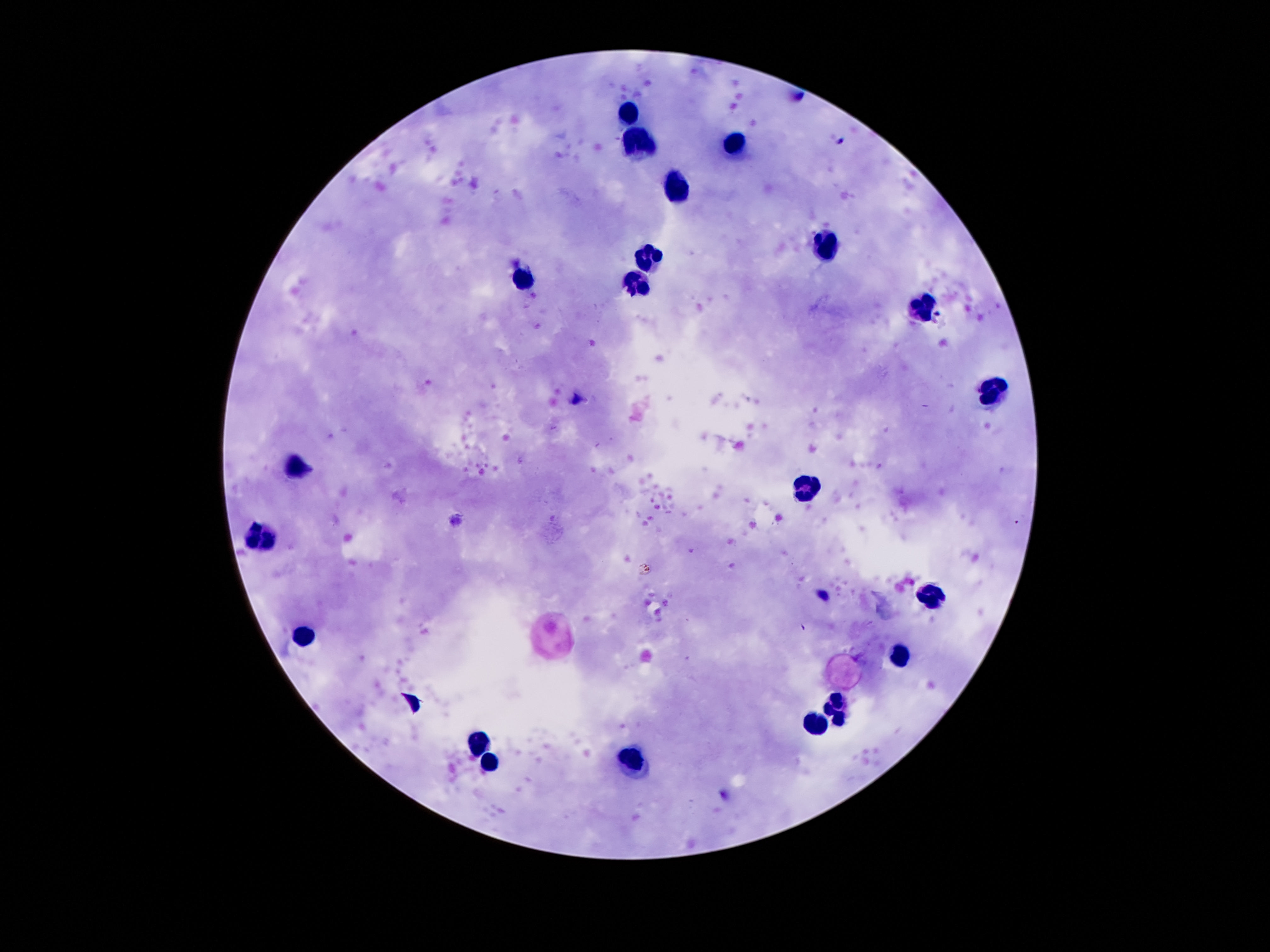
field_of_view: one from this slide
patient_malaria_status: negative
stain: Giemsa
preparation: thick blood film
image_size: 1270×952 pixels
magnification: 100x
leukocyte_locations: 'approximate centers as [x, y] in pixels: [630, 113], [639, 143], [735, 144], [675, 186], [824, 248], [649, 253], [524, 281], [636, 286], [925, 304], [990, 388], [298, 466], [804, 490], [264, 539], [929, 594], [298, 637], [897, 655], [835, 706], [815, 722], [481, 745], [634, 761], [490, 765]'
capture: smartphone camera through the microscope eyepiece